Assess for Plasmodium parasites.
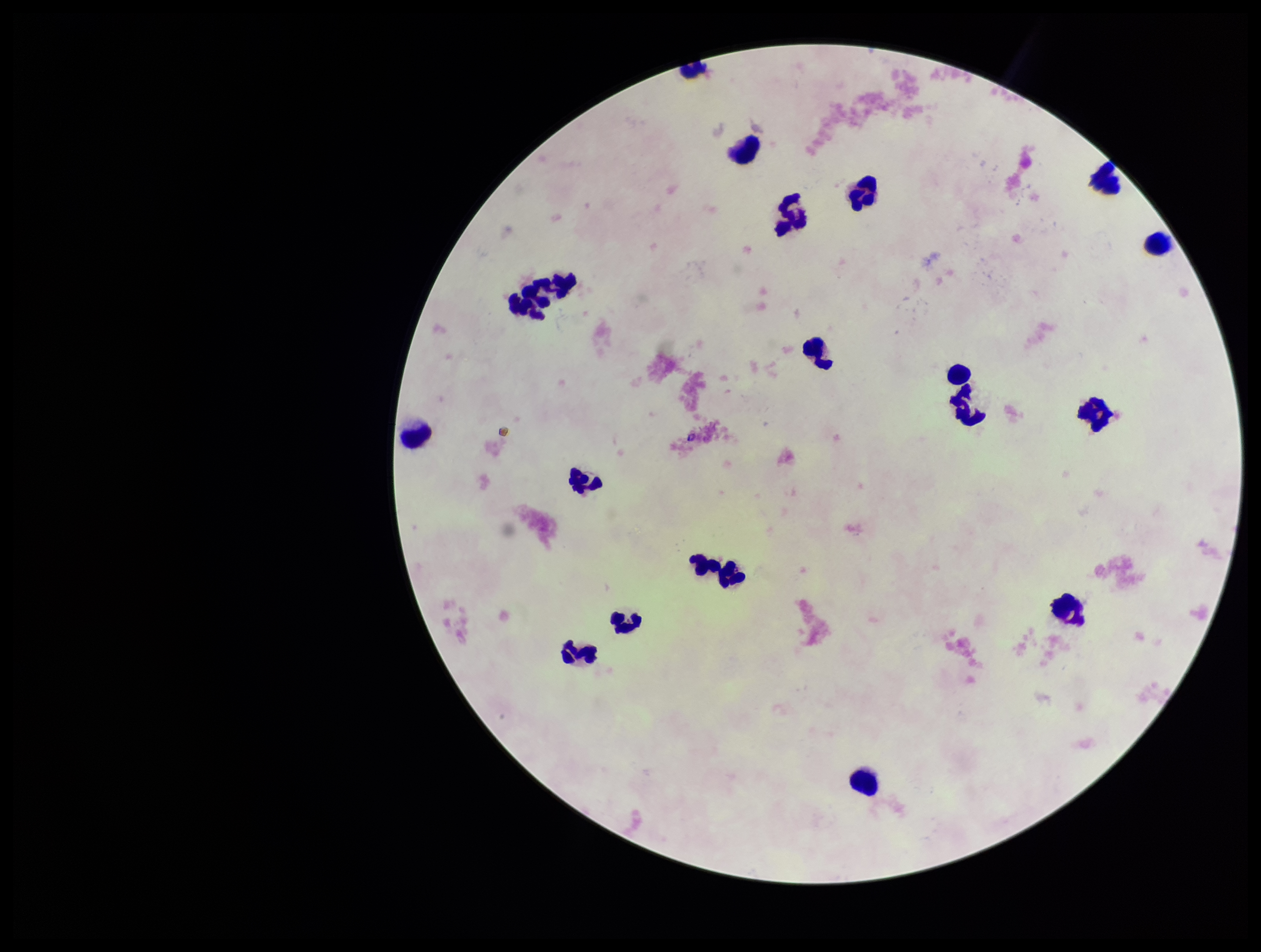
None seen.

field of view = one from this slide
leukocyte count = 20
parasite count = 0
stain = Giemsa
preparation = thick smear
image size = 1261×952 pixels
patient malaria status = negative
capture = smartphone photograph through the microscope eyepiece